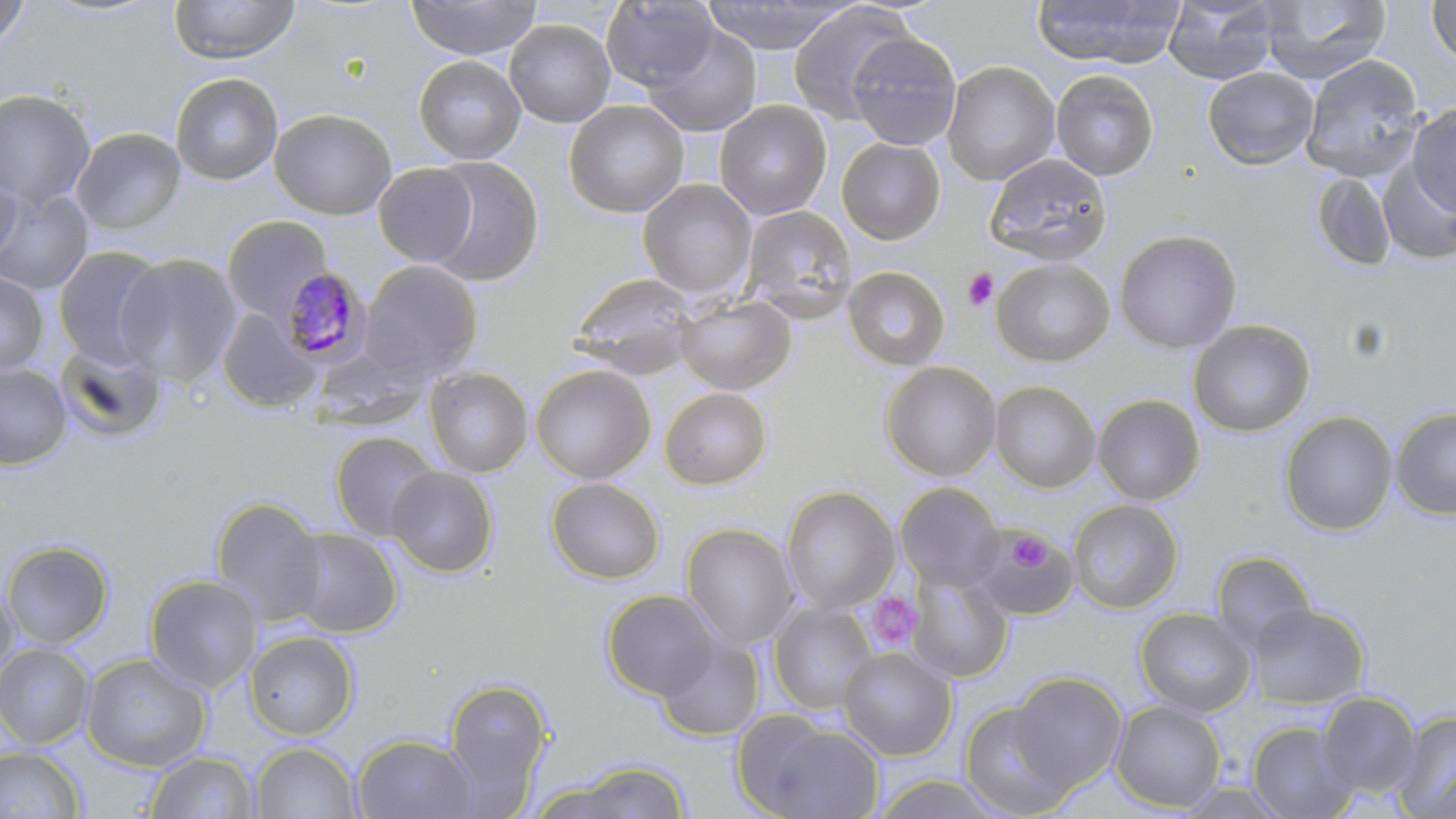
slide-level diagnosis = Plasmodium malariae
platelet locations = approximate bounding boxes as (x1,y1)-(x2,y2) corner pairs in pixels: (962,267)-(999,310), (1008,531)-(1051,573), (864,592)-(922,655)
preparation = thin blood smear
field of view = one of a larger specimen
stain = May-Grünwald-Giemsa
uninfected red blood cell locations = approximate bounding boxes as (x1,y1)-(x2,y2) corner pairs in pixels: (37,0)-(167,20), (169,0)-(299,65), (405,0)-(541,61), (702,0)-(858,54), (1031,0)-(1185,68), (1163,0)-(1279,86), (1257,0)-(1393,84), (0,1)-(33,51), (601,1)-(718,91), (1425,1)-(1456,67), (787,2)-(917,125), (504,19)-(616,128), (640,24)-(762,138), (845,32)-(962,151), (413,55)-(526,164), (1301,55)-(1425,182), (940,60)-(1060,186), (1203,66)-(1319,170), (1050,69)-(1160,181), (170,73)-(283,186), (0,89)-(96,210), (564,99)-(689,218), (714,100)-(832,221), (1406,105)-(1456,217), (269,108)-(397,219), (71,128)-(186,234), (836,137)-(946,244), (983,153)-(1112,265), (424,156)-(544,287), (1377,161)-(1456,265), (373,163)-(478,267), (0,166)-(22,267), (1311,172)-(1397,272), (638,178)-(758,301), (0,188)-(95,295), (740,204)-(858,319), (222,214)-(334,320), (1113,229)-(1242,353), (53,247)-(167,369), (113,254)-(244,386), (991,258)-(1115,367), (358,260)-(484,385), (842,266)-(951,371), (0,271)-(49,375), (569,273)-(699,379), (675,293)-(796,396), (216,309)-(319,414), (1187,319)-(1316,437), (54,341)-(168,445), (309,345)-(430,427), (880,361)-(1001,481), (0,362)-(73,471), (530,364)-(655,484), (423,367)-(534,478), (989,381)-(1100,493), (659,387)-(772,490), (1092,394)-(1206,505), (1390,406)-(1456,520), (1279,411)-(1398,536), (328,431)-(441,541), (387,465)-(499,578), (546,478)-(665,584), (895,482)-(1004,592), (781,486)-(900,614), (210,496)-(329,625), (1067,499)-(1183,613), (681,523)-(799,649), (971,526)-(1078,619), (285,528)-(403,638), (1,540)-(115,650), (1210,551)-(1317,651), (906,569)-(1013,683), (144,574)-(264,693), (0,578)-(18,692), (600,589)-(722,700), (767,602)-(878,716), (1247,603)-(1370,709), (1134,607)-(1256,717), (243,630)-(359,740), (654,633)-(764,742), (0,642)-(95,750), (838,646)-(957,760), (81,652)-(212,772), (1009,672)-(1127,790), (442,677)-(554,806), (1317,692)-(1422,797), (959,700)-(1080,819), (1111,700)-(1226,812), (731,709)-(883,819), (1392,709)-(1456,818), (1246,720)-(1358,818), (351,733)-(479,818), (250,742)-(362,818), (0,746)-(86,818), (144,750)-(258,818), (570,760)-(690,818), (870,772)-(1009,817)
Plasmodium malariae-infected red blood cell locations = approximate bounding boxes as (x1,y1)-(x2,y2) corner pairs in pixels: (277,267)-(373,365)
modality = light microscopy
image size = 1456×819 pixels
magnification = 1000x